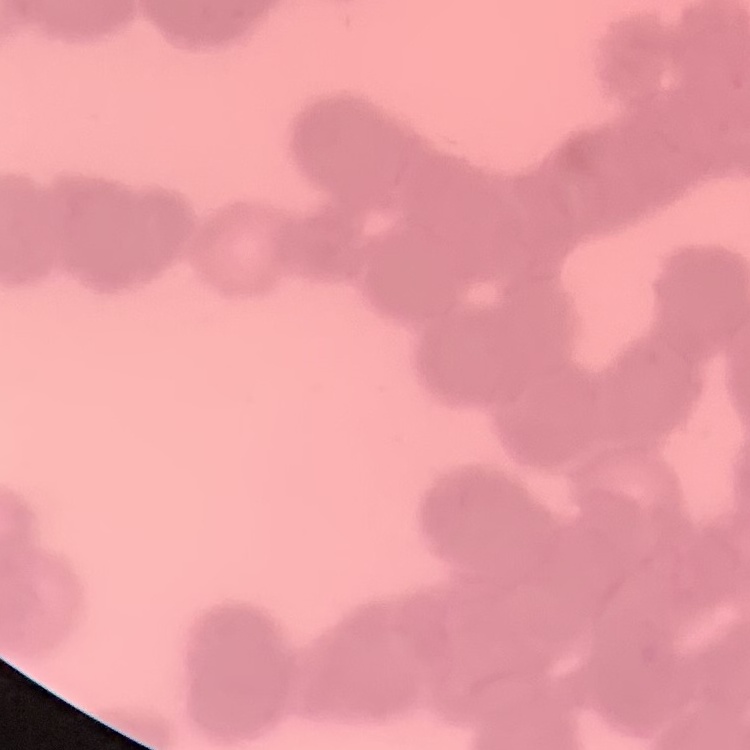
erythrocyte morphology = rouleaux formation
preparation = thin blood smear
image type = square crop of a larger photomicrograph
stain = Field's or Giemsa